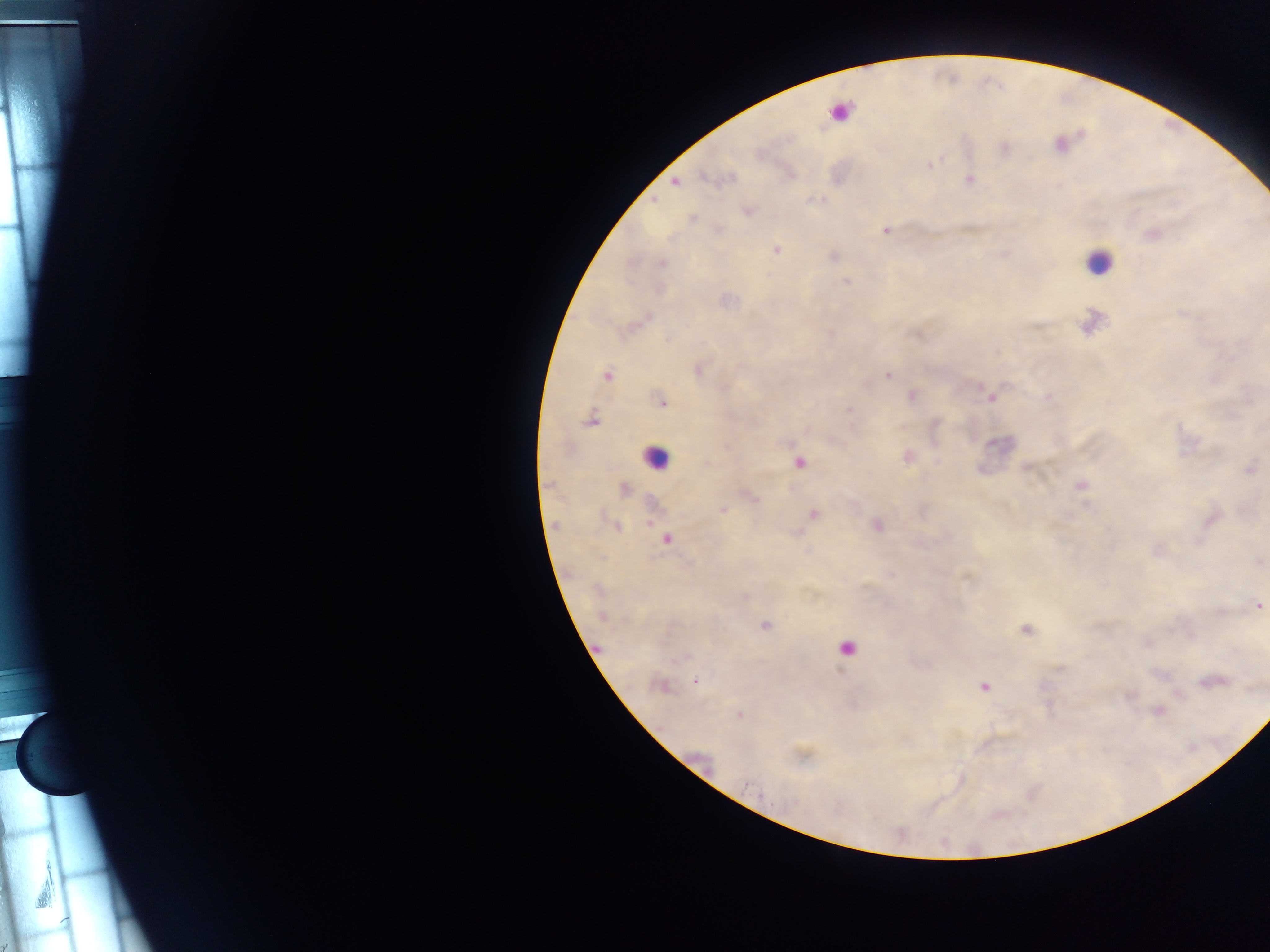

field of view = single
preparation = thick blood smear
image size = 1270×952 pixels
capture = mobile-phone photograph through a microscope
Plasmodium parasite locations = approximate centers as [x, y] in pixels: [929, 164], [970, 179], [675, 183], [809, 199], [655, 204], [885, 229], [775, 249], [833, 256], [663, 263], [847, 280], [726, 299], [831, 332], [698, 370], [608, 375], [887, 375], [911, 394], [1046, 397], [990, 399], [662, 402], [848, 408], [935, 423], [725, 447], [907, 457], [800, 463], [982, 468], [1027, 469], [1081, 484], [626, 490], [752, 496], [723, 511], [814, 516], [649, 521], [876, 526], [617, 528], [797, 534], [666, 540], [893, 575], [967, 577], [744, 596], [1259, 607], [766, 626], [1025, 629], [598, 648], [694, 680], [983, 687], [740, 715], [747, 783]
leukocyte locations = approximate centers as [x, y] in pixels: [1097, 261], [653, 458]
country = Ghana